Identify the blood parasite species.
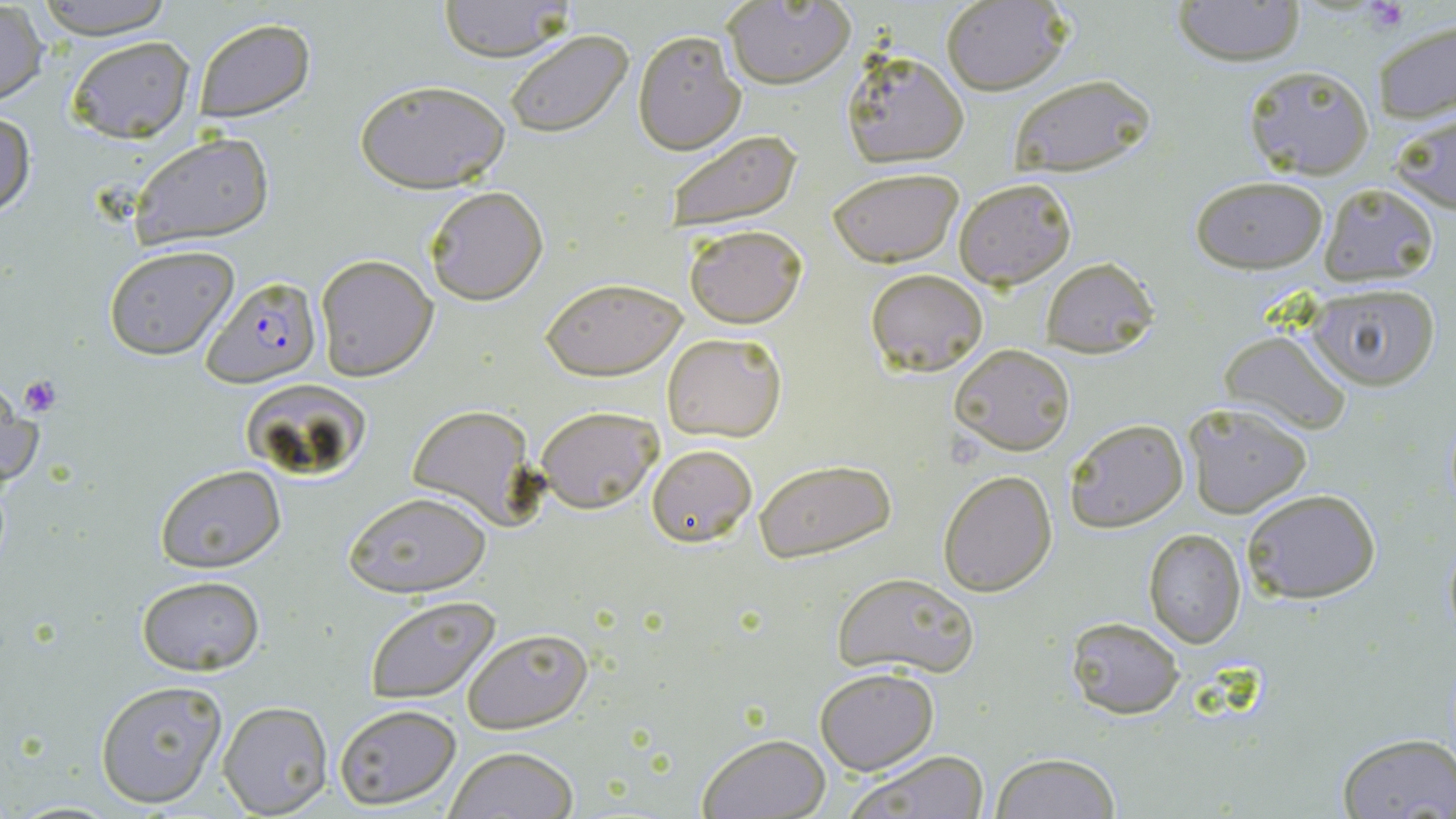

Plasmodium falciparum.

Summary:
  - Coordinate format: approximate bounding boxes as named x1/y1/x2/y2 corners in pixels
  - Plasmodium falciparum-infected red blood cell locations: (x1=202, y1=276, x2=320, y2=387)
  - Uninfected red blood cell locations: (x1=32, y1=0, x2=177, y2=37), (x1=436, y1=0, x2=575, y2=61), (x1=1170, y1=0, x2=1306, y2=66), (x1=939, y1=1, x2=1071, y2=95), (x1=721, y1=2, x2=855, y2=89), (x1=0, y1=4, x2=47, y2=106), (x1=191, y1=17, x2=315, y2=123), (x1=1372, y1=18, x2=1456, y2=125), (x1=632, y1=28, x2=745, y2=155), (x1=504, y1=29, x2=636, y2=138), (x1=64, y1=35, x2=195, y2=144), (x1=840, y1=49, x2=969, y2=167), (x1=1243, y1=65, x2=1375, y2=181), (x1=1005, y1=73, x2=1156, y2=178), (x1=355, y1=78, x2=510, y2=193), (x1=0, y1=109, x2=35, y2=220), (x1=1390, y1=109, x2=1456, y2=214), (x1=660, y1=128, x2=805, y2=236), (x1=129, y1=132, x2=275, y2=249), (x1=827, y1=167, x2=964, y2=267), (x1=953, y1=176, x2=1077, y2=290), (x1=1189, y1=176, x2=1329, y2=274), (x1=1319, y1=183, x2=1440, y2=284), (x1=423, y1=185, x2=549, y2=305), (x1=684, y1=224, x2=809, y2=328), (x1=103, y1=245, x2=240, y2=361), (x1=314, y1=254, x2=438, y2=381), (x1=1039, y1=256, x2=1160, y2=357), (x1=865, y1=269, x2=989, y2=378), (x1=541, y1=277, x2=686, y2=382), (x1=1307, y1=282, x2=1441, y2=389), (x1=1219, y1=328, x2=1353, y2=433), (x1=661, y1=331, x2=788, y2=443), (x1=951, y1=344, x2=1075, y2=456), (x1=1, y1=375, x2=45, y2=492), (x1=1182, y1=401, x2=1313, y2=519), (x1=406, y1=404, x2=536, y2=526), (x1=535, y1=404, x2=663, y2=513), (x1=1063, y1=419, x2=1187, y2=534), (x1=644, y1=443, x2=758, y2=547), (x1=753, y1=459, x2=896, y2=562), (x1=154, y1=463, x2=285, y2=573), (x1=938, y1=471, x2=1057, y2=596), (x1=1241, y1=489, x2=1381, y2=605), (x1=346, y1=494, x2=493, y2=599), (x1=1143, y1=528, x2=1246, y2=648), (x1=1441, y1=529, x2=1456, y2=644), (x1=830, y1=570, x2=979, y2=678), (x1=135, y1=576, x2=265, y2=676), (x1=362, y1=595, x2=500, y2=704), (x1=1064, y1=616, x2=1185, y2=719), (x1=463, y1=628, x2=592, y2=735), (x1=815, y1=666, x2=938, y2=775), (x1=95, y1=680, x2=228, y2=807), (x1=218, y1=701, x2=332, y2=816), (x1=335, y1=705, x2=461, y2=810), (x1=698, y1=732, x2=832, y2=818), (x1=1336, y1=732, x2=1455, y2=817), (x1=444, y1=746, x2=578, y2=819), (x1=848, y1=749, x2=990, y2=818), (x1=990, y1=752, x2=1120, y2=819)
  - Platelet locations: (x1=1363, y1=0, x2=1407, y2=30), (x1=18, y1=375, x2=63, y2=418)
  - Image size: 1456×819 pixels
  - Stain: May-Grünwald-Giemsa
  - Magnification: 1000x
  - Preparation: thin blood smear
  - Field of view: one of a larger specimen
  - Modality: optical microscopy